Assess this cell for malaria.
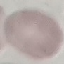
It is uninfected.

Summary:
  - Capture: smartphone camera at the microscope eyepiece
  - Preparation: thin blood smear
  - Image type: automatically extracted cell patch, resized to 64 × 64 pixels
  - Stain: Giemsa